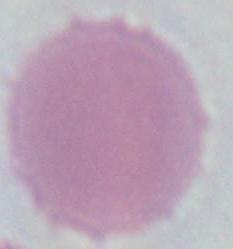
Photomicrograph. 1000x magnification. A red blood cell is shown.